Outline each blood parasite and name the species.
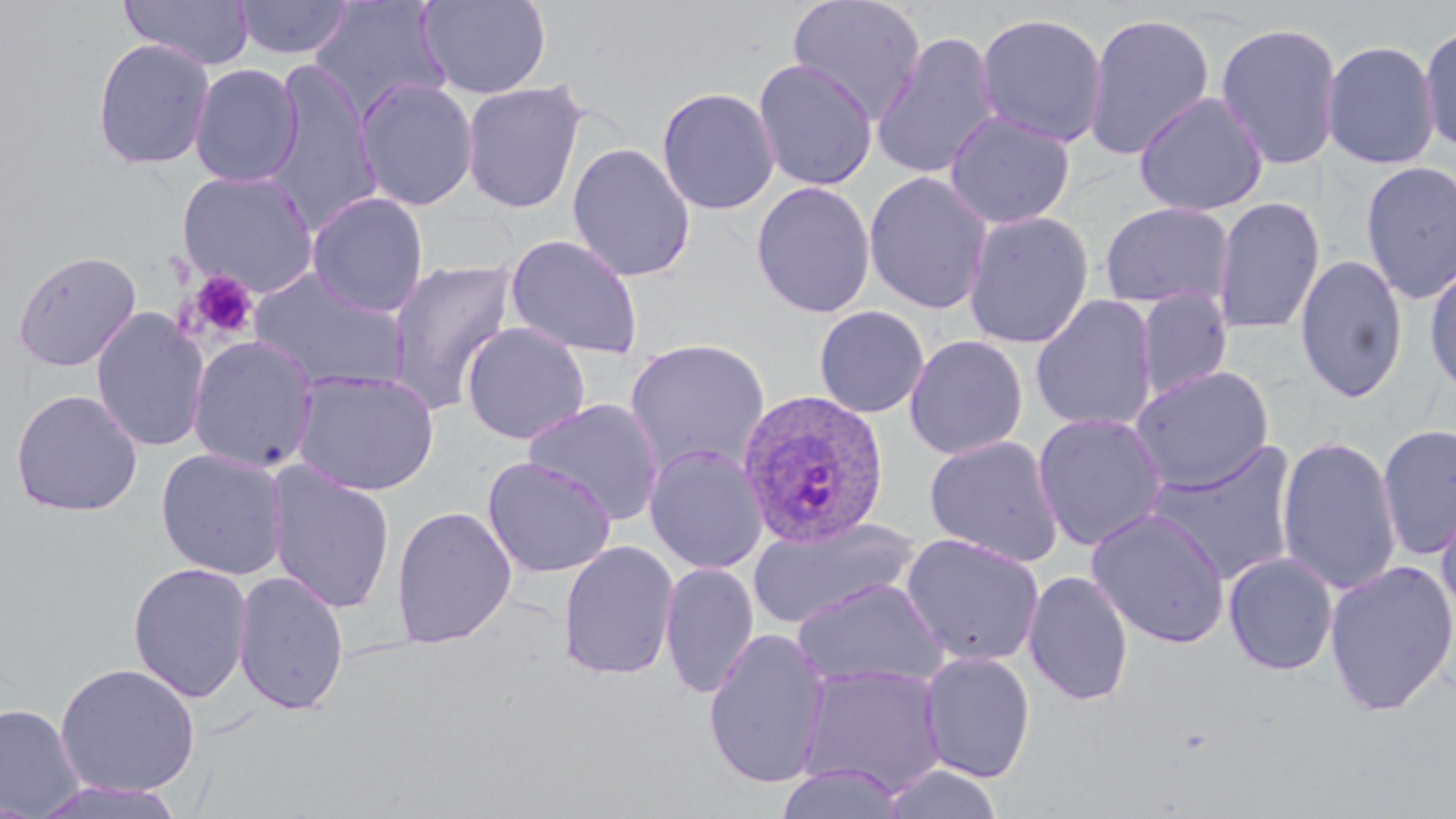

Approximate bounding boxes as [x1, y1, x2, y2] in pixels.
Plasmodium ovale-infected red blood cells: [737, 389, 892, 550].
No Plasmodium falciparum, Plasmodium malariae, Plasmodium vivax, Babesia divergens, or Trypanosoma brucei observed.

Uninfected red blood cell locations: [120, 0, 255, 70], [233, 0, 353, 60], [417, 0, 551, 100], [787, 0, 928, 124], [309, 1, 451, 124], [430, 2, 561, 191], [974, 11, 1108, 148], [1083, 11, 1215, 161], [1214, 21, 1344, 171], [1419, 21, 1456, 156], [870, 30, 1003, 181], [92, 38, 215, 170], [1321, 38, 1440, 170], [753, 58, 878, 191], [262, 61, 382, 235], [189, 63, 303, 187], [355, 78, 479, 211], [461, 81, 587, 214], [656, 87, 780, 216], [1134, 90, 1269, 218], [944, 110, 1076, 229], [567, 142, 695, 283], [1360, 160, 1456, 305], [178, 168, 320, 298], [863, 171, 993, 315], [751, 181, 876, 319], [306, 192, 429, 317], [1211, 195, 1325, 336], [1099, 202, 1234, 310], [963, 210, 1094, 349], [505, 234, 644, 360], [12, 249, 142, 372], [1294, 253, 1409, 405], [1423, 257, 1456, 399], [387, 259, 518, 414], [246, 267, 409, 395], [1134, 289, 1233, 401], [1030, 294, 1158, 433], [813, 306, 929, 418], [91, 307, 211, 453], [460, 322, 591, 445], [904, 334, 1028, 460], [187, 335, 319, 473], [624, 338, 771, 478], [1129, 365, 1274, 493], [291, 369, 441, 497], [10, 389, 144, 517], [524, 398, 665, 526], [1032, 412, 1168, 552], [1376, 422, 1456, 560], [924, 434, 1065, 568], [1276, 435, 1402, 596], [1144, 440, 1299, 586], [645, 444, 769, 575], [155, 448, 289, 580], [482, 456, 617, 578], [266, 461, 396, 614], [1434, 492, 1456, 636], [391, 505, 517, 647], [1086, 507, 1231, 648], [748, 515, 920, 630], [900, 533, 1045, 667], [558, 539, 680, 682], [1223, 552, 1339, 676], [1323, 559, 1456, 716], [127, 561, 253, 703], [659, 562, 760, 700], [233, 569, 350, 717], [1023, 570, 1135, 707], [790, 577, 949, 691], [702, 628, 831, 789], [918, 651, 1036, 782], [54, 662, 201, 797], [796, 663, 947, 798], [0, 703, 85, 818], [879, 763, 1005, 819], [775, 765, 907, 819], [28, 779, 189, 818]. Platelet locations: [186, 270, 258, 342]. Slide-level diagnosis: Plasmodium ovale. May-Grünwald-Giemsa stain. Optical microscopy. Captured at 1000x magnification. Thin blood smear. Single field of view. Image is 1456×819 pixels.